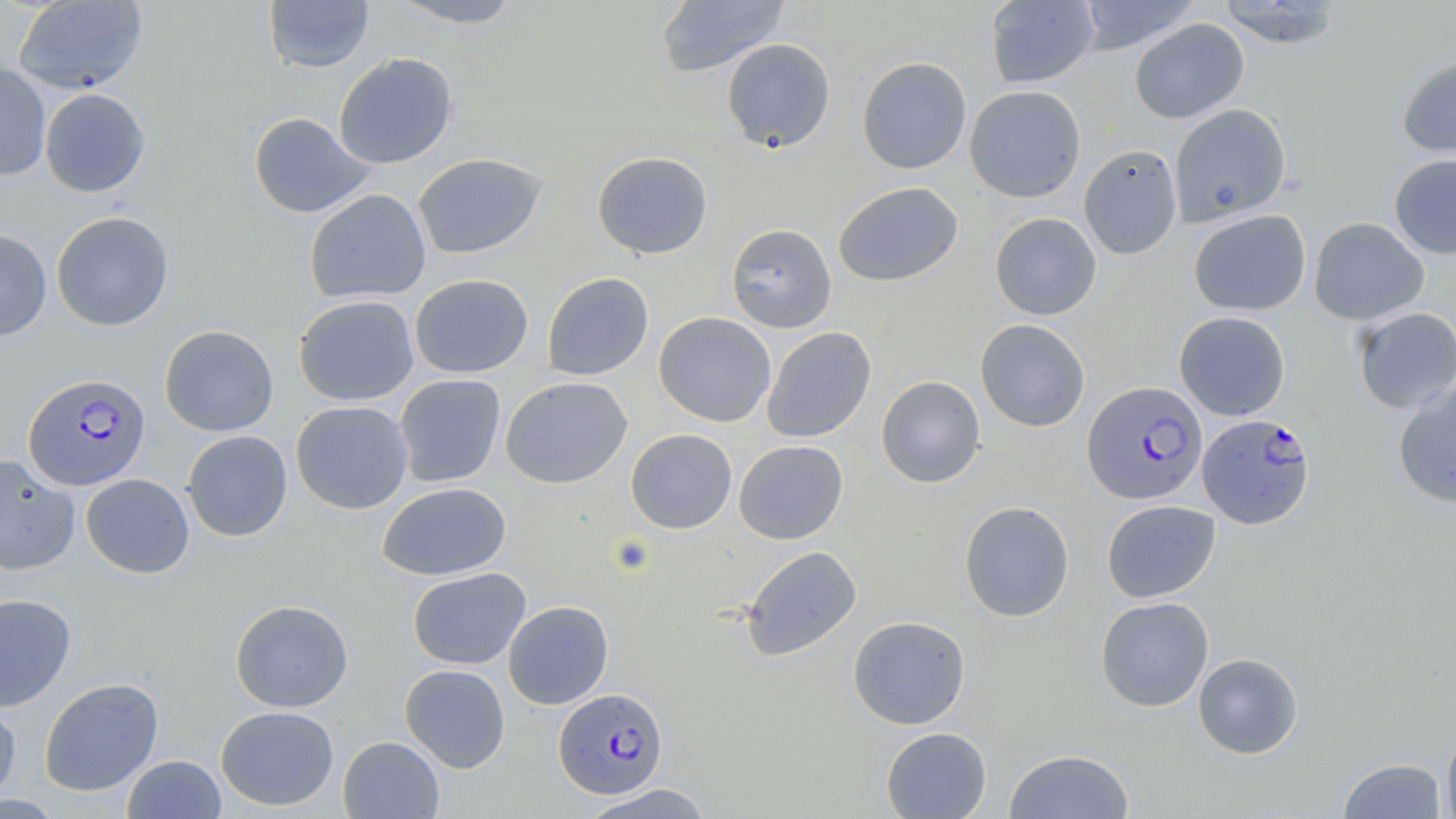

Summary:
  - Coordinate format: approximate bounding boxes as [x1, y1, x2, y2] in pixels
  - Plasmodium falciparum-infected red blood cell locations: [23, 373, 151, 490], [1082, 380, 1207, 504], [1197, 414, 1315, 529], [553, 687, 669, 800]
  - Platelet locations: [608, 534, 657, 577]
  - Uninfected red blood cell locations: [13, 0, 148, 94], [264, 0, 375, 74], [386, 0, 527, 29], [655, 0, 790, 78], [1074, 0, 1202, 54], [984, 1, 1100, 88], [1213, 1, 1348, 49], [1130, 18, 1249, 123], [721, 38, 836, 153], [333, 53, 457, 169], [1396, 55, 1456, 161], [856, 56, 972, 174], [0, 63, 51, 181], [964, 85, 1086, 202], [39, 88, 151, 197], [1169, 104, 1291, 226], [248, 112, 375, 218], [1078, 143, 1183, 259], [592, 151, 713, 259], [1388, 152, 1456, 259], [412, 153, 546, 259], [833, 181, 963, 287], [304, 189, 431, 303], [1188, 209, 1311, 316], [51, 211, 174, 331], [990, 212, 1102, 320], [1308, 217, 1430, 325], [726, 223, 837, 333], [0, 229, 52, 342], [542, 272, 654, 380], [410, 274, 533, 378], [293, 294, 419, 406], [1352, 307, 1456, 413], [653, 311, 776, 427], [1174, 311, 1291, 420], [975, 319, 1090, 432], [159, 325, 279, 436], [761, 327, 876, 443], [393, 374, 506, 487], [876, 375, 985, 488], [501, 376, 632, 488], [1392, 380, 1456, 508], [290, 400, 413, 514], [625, 428, 737, 534], [182, 430, 293, 541], [734, 440, 848, 544], [0, 453, 80, 575], [81, 474, 195, 578], [377, 482, 512, 581], [959, 500, 1074, 622], [1102, 500, 1221, 602], [740, 545, 862, 661], [407, 567, 531, 670], [0, 593, 76, 712], [1095, 596, 1214, 711], [230, 598, 354, 712], [502, 600, 614, 709], [848, 615, 971, 729], [1193, 652, 1304, 759], [399, 664, 510, 773], [39, 677, 164, 796], [0, 700, 21, 805], [216, 705, 339, 811], [1441, 720, 1456, 819], [880, 727, 992, 818], [337, 735, 445, 818], [1004, 749, 1135, 819], [122, 754, 226, 818], [1336, 757, 1448, 818], [577, 783, 716, 819]
  - Slide-level diagnosis: Plasmodium falciparum
  - Modality: optical microscopy
  - Stain: May-Grünwald-Giemsa
  - Magnification: 1000x
  - Preparation: thin blood smear
  - Image size: 1456×819 pixels
  - Field of view: one of a larger specimen